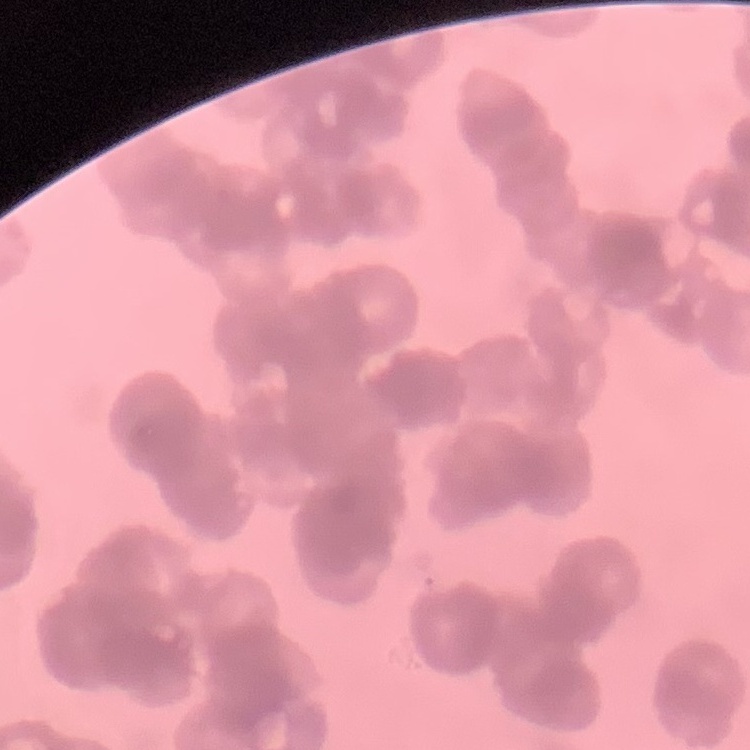

{
  "red_blood_cell_morphology": "rouleaux formation",
  "preparation": "thin peripheral smear",
  "stain": "Field's or Giemsa",
  "image_type": "square crop of a larger photomicrograph"
}